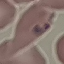
Summary:
  - Malaria status: parasitized
  - Preparation: thin blood smear
  - Image type: automatically extracted cell patch, resized to 64 × 64 pixels
  - Capture: smartphone camera at the microscope eyepiece
  - Stain: Giemsa